Classify this cell by malaria status.
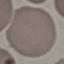

It is uninfected.

capture: smartphone through the microscope eyepiece
stain: Giemsa
image_type: automatically extracted cell patch, resized to 64 × 64 pixels
preparation: thin blood smear